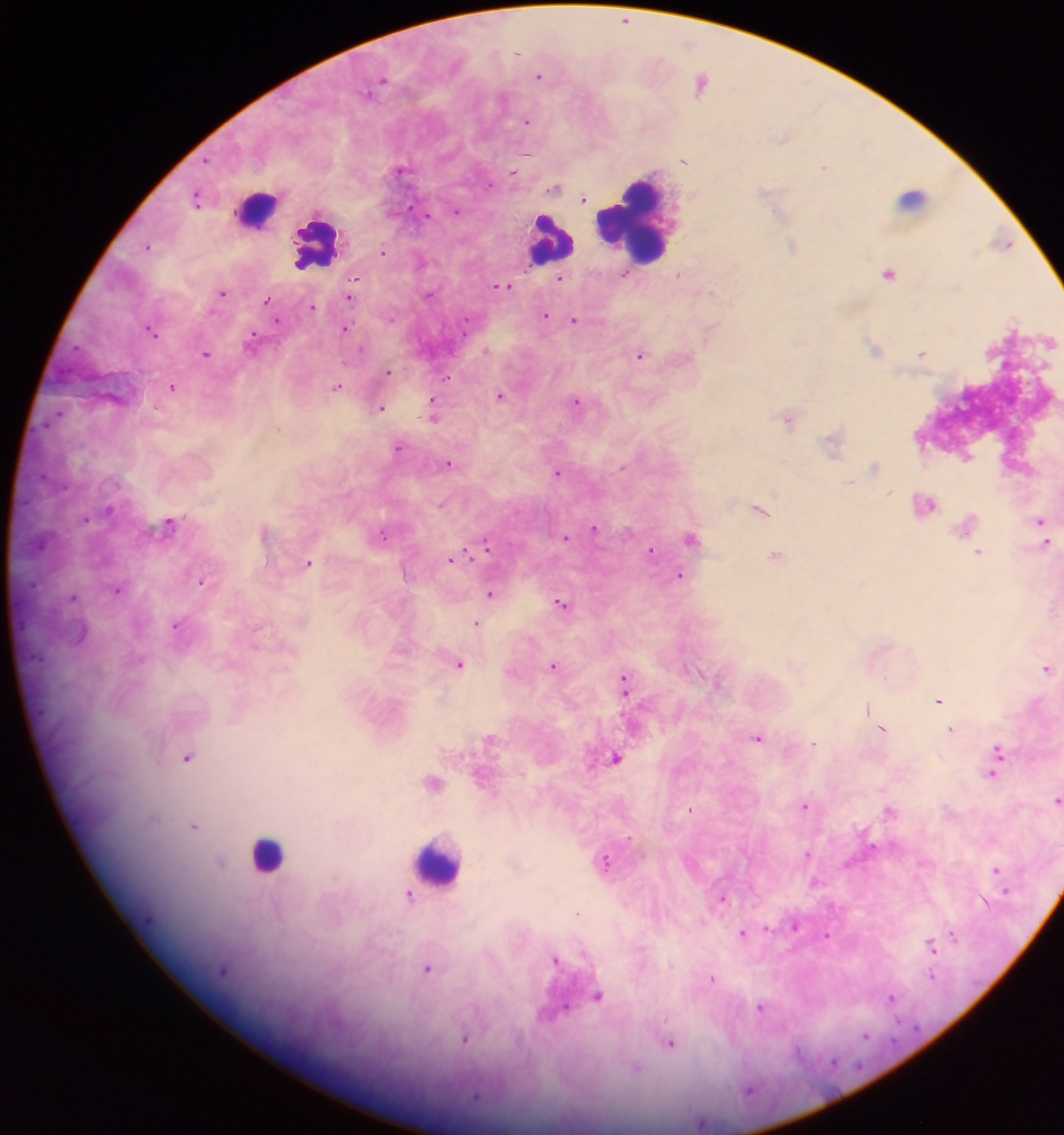
image_size: 1064×1135 pixels
preparation: thick blood smear
plasmodium_parasite_locations: 'approximate centers as (x, y) in pixels: (626, 21), (539, 76), (383, 80), (703, 82), (528, 121), (684, 161), (825, 165), (401, 169), (556, 187), (198, 198), (585, 198), (457, 211), (1005, 243), (148, 246), (793, 247), (383, 252), (890, 272), (625, 275), (561, 278), (503, 285), (223, 292), (350, 297), (269, 301), (314, 307), (545, 315), (276, 319), (574, 319), (345, 328), (152, 330), (252, 340), (875, 346), (923, 353), (206, 354), (641, 355), (389, 371), (173, 387), (337, 387), (502, 395), (578, 401), (381, 407), (434, 410), (790, 418), (835, 441), (400, 447), (449, 462), (876, 465), (559, 472), (889, 492), (926, 505), (762, 509), (1042, 520), (170, 522), (967, 523), (596, 528), (266, 532), (383, 534), (566, 538), (692, 538), (1046, 542), (487, 545), (652, 550), (979, 552), (778, 556), (454, 559), (309, 563), (680, 575), (202, 581), (119, 589), (492, 593), (74, 597), (562, 603), (477, 623), (178, 625), (460, 663), (554, 665), (1049, 668), (625, 682), (940, 700), (868, 708), (885, 729), (952, 729), (759, 738), (491, 739), (814, 743), (998, 755), (189, 757), (616, 758), (995, 770), (434, 781), (1058, 799), (807, 805), (692, 810), (892, 810), (195, 826), (808, 854), (607, 862), (997, 870), (817, 882), (1006, 890), (410, 894), (723, 898), (985, 900), (579, 912), (797, 925), (744, 933), (953, 935), (826, 936), (932, 945), (557, 960), (429, 968), (933, 976), (713, 978), (599, 996), (893, 998), (762, 1006), (466, 1038), (671, 1043), (636, 1069), (749, 1090), (703, 1122)'
country: Ghana
leukocyte_locations: 'approximate centers as (x, y) in pixels: (914, 199), (256, 207), (635, 221), (552, 240), (317, 244), (267, 854), (439, 861)'
capture: mobile-phone photograph through a microscope
field_of_view: single